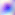

Summary:
  - Magnification: 400x
  - Identification: Toxoplasma gondii
  - Modality: photomicrograph